Locate every Plasmodium falciparum-infected red blood cell.
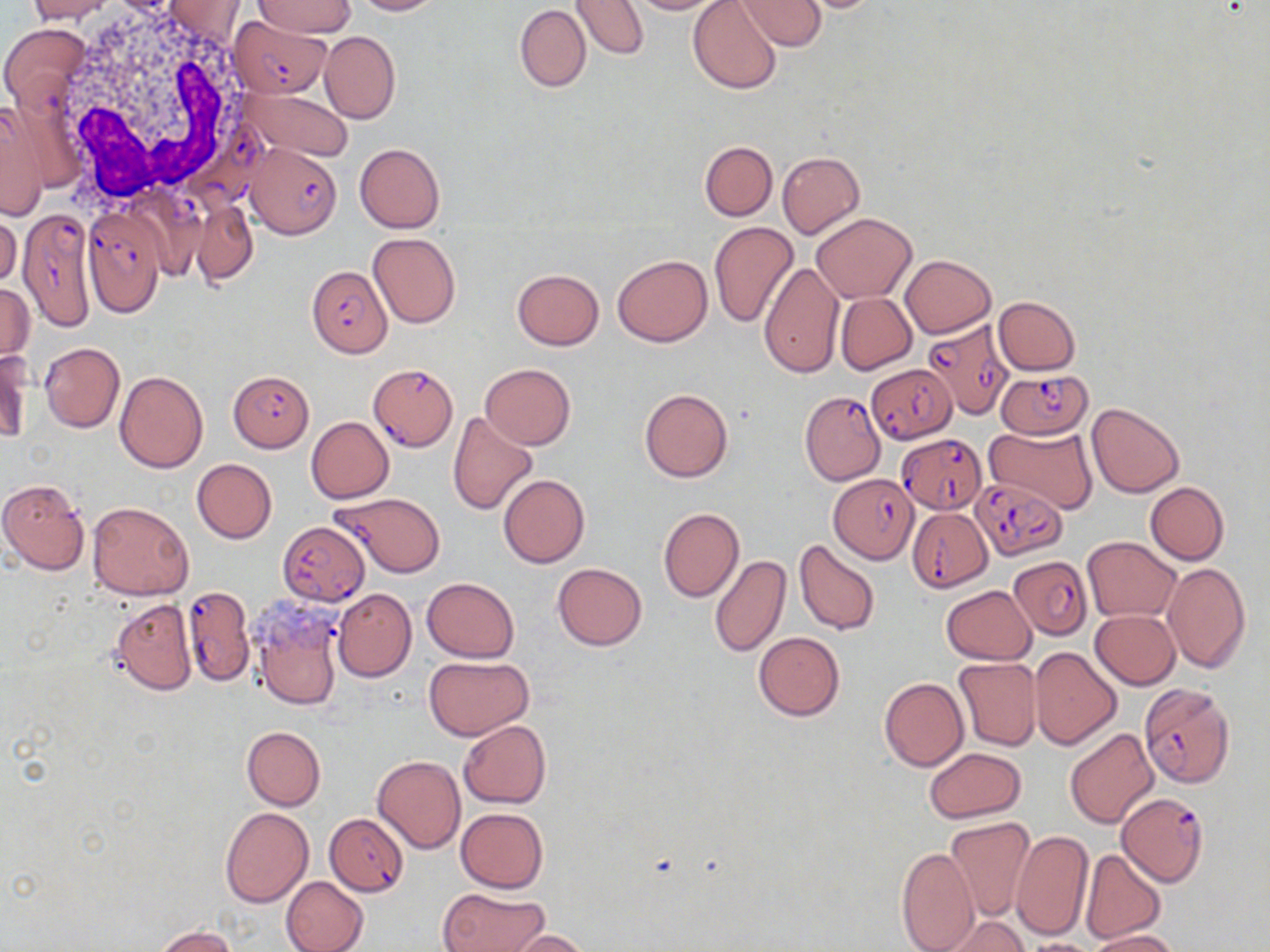
Approximate bounding boxes as named x1/y1/x2/y2 corners in pixels.
Plasmodium falciparum-infected red blood cells: (x1=230, y1=15, x2=328, y2=97), (x1=196, y1=122, x2=272, y2=218), (x1=244, y1=143, x2=342, y2=238), (x1=83, y1=211, x2=167, y2=317), (x1=18, y1=213, x2=95, y2=327), (x1=306, y1=262, x2=392, y2=358), (x1=921, y1=318, x2=1018, y2=418), (x1=866, y1=364, x2=958, y2=443), (x1=369, y1=365, x2=457, y2=451), (x1=231, y1=370, x2=311, y2=450), (x1=996, y1=370, x2=1093, y2=438), (x1=800, y1=389, x2=888, y2=486), (x1=899, y1=434, x2=986, y2=512), (x1=828, y1=474, x2=918, y2=563), (x1=974, y1=478, x2=1069, y2=561), (x1=332, y1=492, x2=445, y2=578), (x1=908, y1=508, x2=992, y2=591), (x1=278, y1=520, x2=370, y2=605), (x1=1009, y1=555, x2=1092, y2=640), (x1=182, y1=587, x2=254, y2=685), (x1=1140, y1=683, x2=1235, y2=787), (x1=1117, y1=792, x2=1209, y2=886), (x1=324, y1=813, x2=409, y2=896).

slide-level diagnosis = Plasmodium falciparum
white blood cell locations = approximate bounding boxes as named x1/y1/x2/y2 corners in pixels: (x1=50, y1=5, x2=263, y2=208)
stain = May-Grünwald-Giemsa
uninfected red blood cell locations = approximate bounding boxes as named x1/y1/x2/y2 corners in pixels: (x1=26, y1=0, x2=115, y2=23), (x1=350, y1=0, x2=446, y2=16), (x1=571, y1=0, x2=647, y2=59), (x1=625, y1=0, x2=725, y2=14), (x1=735, y1=0, x2=826, y2=51), (x1=790, y1=0, x2=890, y2=13), (x1=162, y1=1, x2=245, y2=42), (x1=254, y1=1, x2=355, y2=38), (x1=688, y1=1, x2=782, y2=94), (x1=514, y1=4, x2=591, y2=93), (x1=1, y1=24, x2=90, y2=110), (x1=320, y1=31, x2=400, y2=125), (x1=237, y1=86, x2=354, y2=162), (x1=0, y1=104, x2=47, y2=221), (x1=700, y1=141, x2=777, y2=221), (x1=354, y1=143, x2=445, y2=232), (x1=777, y1=151, x2=865, y2=239), (x1=192, y1=202, x2=258, y2=284), (x1=0, y1=209, x2=21, y2=288), (x1=813, y1=213, x2=917, y2=303), (x1=709, y1=222, x2=799, y2=328), (x1=368, y1=233, x2=461, y2=329), (x1=613, y1=254, x2=713, y2=346), (x1=900, y1=255, x2=996, y2=338), (x1=758, y1=262, x2=844, y2=379), (x1=506, y1=266, x2=597, y2=430), (x1=511, y1=269, x2=605, y2=350), (x1=0, y1=283, x2=33, y2=364), (x1=836, y1=293, x2=916, y2=374), (x1=993, y1=296, x2=1080, y2=375), (x1=40, y1=342, x2=125, y2=432), (x1=0, y1=349, x2=31, y2=445), (x1=479, y1=364, x2=576, y2=449), (x1=115, y1=370, x2=209, y2=473), (x1=638, y1=388, x2=733, y2=482), (x1=1087, y1=402, x2=1185, y2=497), (x1=447, y1=411, x2=538, y2=516), (x1=306, y1=417, x2=393, y2=502), (x1=985, y1=426, x2=1097, y2=514), (x1=191, y1=459, x2=276, y2=544), (x1=498, y1=473, x2=589, y2=567), (x1=0, y1=479, x2=91, y2=576), (x1=1145, y1=482, x2=1230, y2=564), (x1=86, y1=501, x2=194, y2=601), (x1=657, y1=508, x2=744, y2=601), (x1=1082, y1=536, x2=1180, y2=622), (x1=793, y1=540, x2=879, y2=636), (x1=710, y1=556, x2=790, y2=658), (x1=1161, y1=562, x2=1252, y2=673), (x1=552, y1=563, x2=648, y2=651), (x1=422, y1=577, x2=519, y2=662), (x1=941, y1=585, x2=1036, y2=664), (x1=334, y1=589, x2=417, y2=682), (x1=111, y1=599, x2=197, y2=695), (x1=250, y1=599, x2=346, y2=713), (x1=1091, y1=609, x2=1181, y2=689), (x1=753, y1=631, x2=845, y2=721), (x1=1030, y1=647, x2=1122, y2=749), (x1=424, y1=656, x2=533, y2=740), (x1=953, y1=658, x2=1042, y2=751), (x1=879, y1=678, x2=968, y2=771), (x1=458, y1=721, x2=551, y2=808), (x1=241, y1=726, x2=325, y2=810), (x1=1066, y1=728, x2=1159, y2=828), (x1=924, y1=747, x2=1027, y2=823), (x1=373, y1=754, x2=465, y2=854), (x1=218, y1=807, x2=313, y2=908), (x1=456, y1=808, x2=548, y2=893), (x1=944, y1=816, x2=1035, y2=921), (x1=1011, y1=829, x2=1093, y2=943), (x1=896, y1=845, x2=979, y2=952), (x1=1078, y1=848, x2=1166, y2=944), (x1=281, y1=876, x2=369, y2=952), (x1=438, y1=887, x2=549, y2=952), (x1=937, y1=914, x2=1033, y2=952), (x1=153, y1=926, x2=236, y2=952), (x1=1087, y1=929, x2=1181, y2=952), (x1=505, y1=930, x2=594, y2=951), (x1=1021, y1=938, x2=1103, y2=952)
image size = 1270×952 pixels
magnification = 1000x
modality = light microscopy
preparation = thin blood film
field of view = single